Classify this cell by malaria status.
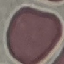
It is uninfected.

Thin smear of blood. Giemsa-stained preparation. Automatically extracted cell patch, resized to 64 × 64 pixels. Acquired by smartphone through the microscope eyepiece.